Report the malaria status of this cell.
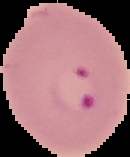
Parasitized.

Summary:
  - Image type: segmented cell region with the area outside set to black
  - Image size: 130×157 pixels
  - Preparation: thin blood film